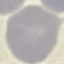

malaria_status: uninfected
stain: Giemsa
preparation: thin blood smear
image_type: automatically extracted cell patch, resized to 64 × 64 pixels
capture: smartphone through the microscope eyepiece